Assess this cell for malaria.
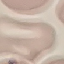
Uninfected.

Summary:
  - Image type: cell patch, automatically extracted from a larger field of view and resized to 64 × 64 pixels
  - Stain: Giemsa
  - Capture: smartphone camera at the microscope eyepiece
  - Preparation: thin blood film